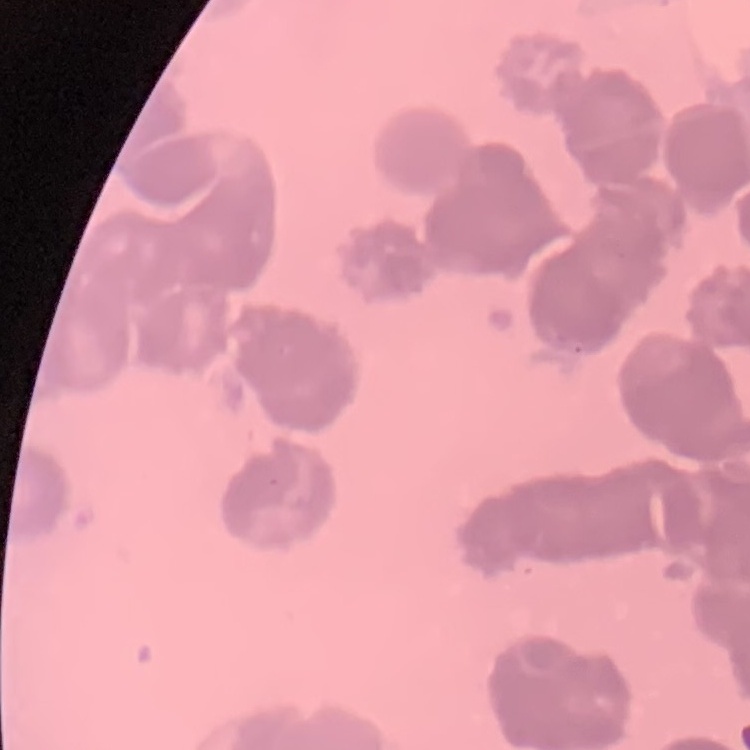

{
  "erythrocyte_morphology": "rouleaux formation",
  "preparation": "thin peripheral smear",
  "image_type": "one tile cut from a larger photomicrograph",
  "stain": "Field's or Giemsa"
}